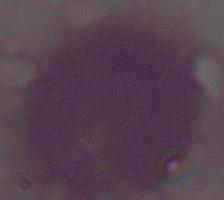
magnification = 1000x
modality = photomicrograph
identification = red blood cell